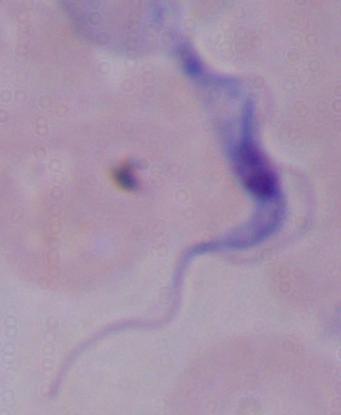 Micrograph. A trypanosome is seen. Captured at 1000x magnification.